Name the blood parasite species.
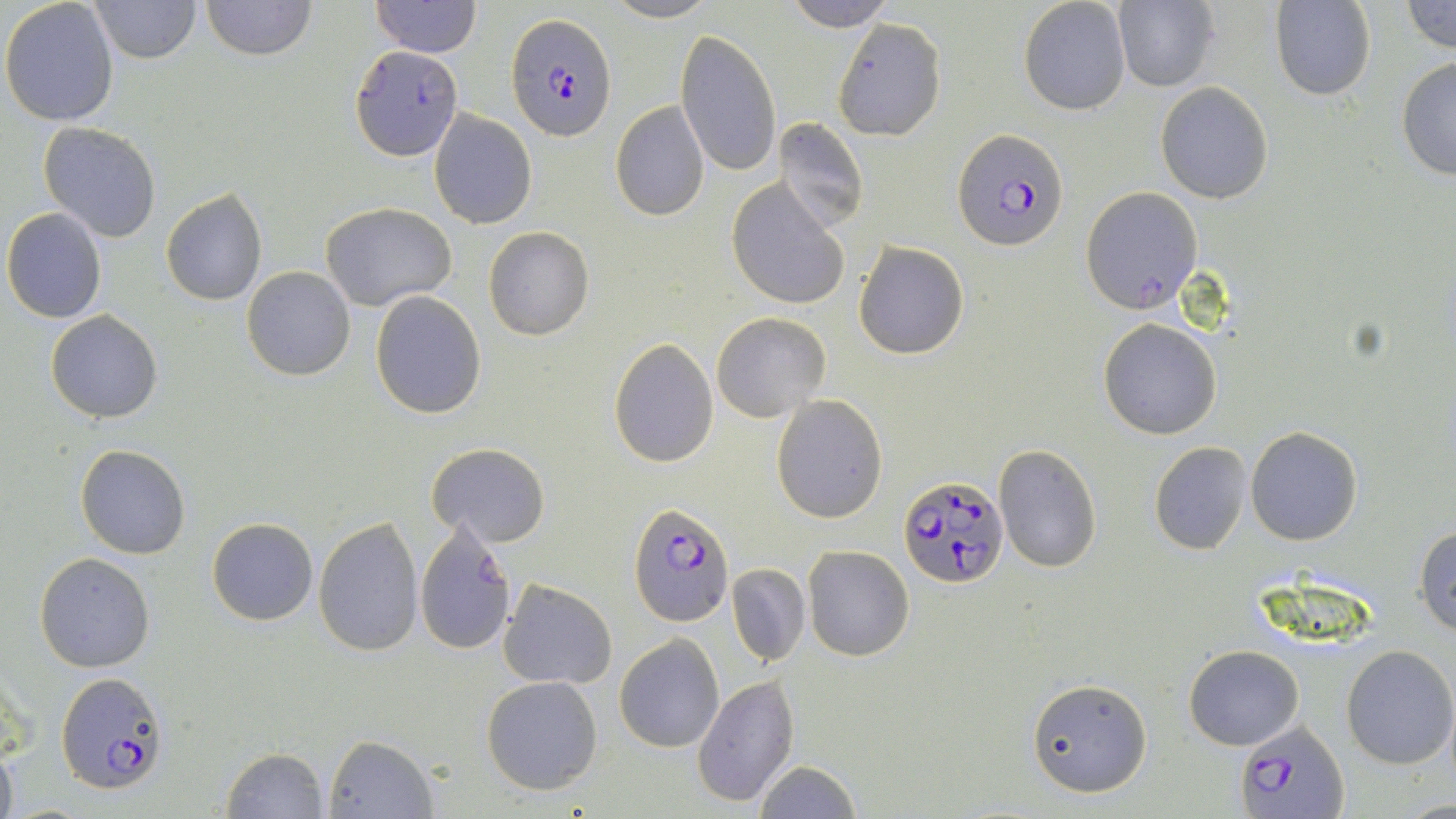

Plasmodium falciparum.

Approximate bounding boxes as named x1/y1/x2/y2 corners in pixels. Uninfected red blood cell locations: (x1=0, y1=0, x2=122, y2=125), (x1=90, y1=0, x2=200, y2=63), (x1=201, y1=0, x2=315, y2=60), (x1=370, y1=0, x2=482, y2=58), (x1=603, y1=0, x2=718, y2=24), (x1=1018, y1=0, x2=1132, y2=116), (x1=1112, y1=0, x2=1219, y2=91), (x1=785, y1=1, x2=895, y2=31), (x1=1271, y1=1, x2=1375, y2=101), (x1=1401, y1=1, x2=1456, y2=53), (x1=832, y1=17, x2=947, y2=141), (x1=675, y1=29, x2=784, y2=179), (x1=1395, y1=53, x2=1456, y2=181), (x1=1155, y1=82, x2=1273, y2=204), (x1=609, y1=100, x2=711, y2=221), (x1=428, y1=111, x2=537, y2=228), (x1=774, y1=117, x2=868, y2=232), (x1=38, y1=122, x2=162, y2=243), (x1=726, y1=179, x2=851, y2=312), (x1=1081, y1=186, x2=1202, y2=313), (x1=160, y1=188, x2=267, y2=307), (x1=321, y1=202, x2=457, y2=311), (x1=2, y1=208, x2=107, y2=322), (x1=483, y1=227, x2=595, y2=341), (x1=852, y1=240, x2=969, y2=360), (x1=242, y1=267, x2=356, y2=380), (x1=370, y1=291, x2=488, y2=418), (x1=46, y1=310, x2=162, y2=423), (x1=711, y1=312, x2=830, y2=421), (x1=1098, y1=317, x2=1223, y2=440), (x1=609, y1=338, x2=718, y2=467), (x1=771, y1=395, x2=888, y2=523), (x1=1246, y1=427, x2=1363, y2=546), (x1=1148, y1=440, x2=1253, y2=555), (x1=75, y1=443, x2=192, y2=560), (x1=426, y1=443, x2=551, y2=547), (x1=993, y1=444, x2=1101, y2=574), (x1=314, y1=515, x2=425, y2=656), (x1=206, y1=518, x2=318, y2=625), (x1=413, y1=520, x2=518, y2=653), (x1=1413, y1=524, x2=1456, y2=636), (x1=802, y1=546, x2=916, y2=661), (x1=34, y1=552, x2=156, y2=673), (x1=728, y1=564, x2=809, y2=666), (x1=498, y1=579, x2=617, y2=690), (x1=614, y1=634, x2=724, y2=752), (x1=1184, y1=644, x2=1304, y2=750), (x1=1339, y1=644, x2=1455, y2=769), (x1=693, y1=674, x2=800, y2=807), (x1=481, y1=675, x2=603, y2=794), (x1=1028, y1=677, x2=1152, y2=797), (x1=324, y1=734, x2=438, y2=817), (x1=0, y1=744, x2=17, y2=819), (x1=221, y1=747, x2=329, y2=819), (x1=752, y1=760, x2=861, y2=819). Plasmodium falciparum-infected red blood cell locations: (x1=505, y1=12, x2=617, y2=140), (x1=349, y1=46, x2=463, y2=161), (x1=955, y1=128, x2=1069, y2=251), (x1=899, y1=474, x2=1010, y2=589), (x1=630, y1=503, x2=733, y2=627), (x1=59, y1=672, x2=171, y2=794), (x1=1238, y1=721, x2=1346, y2=819). Captured at 1000x magnification. May-Grünwald-Giemsa-stained preparation. Light microscopy. Thin blood smear. Image is 1456×819 pixels. One field of a larger specimen.